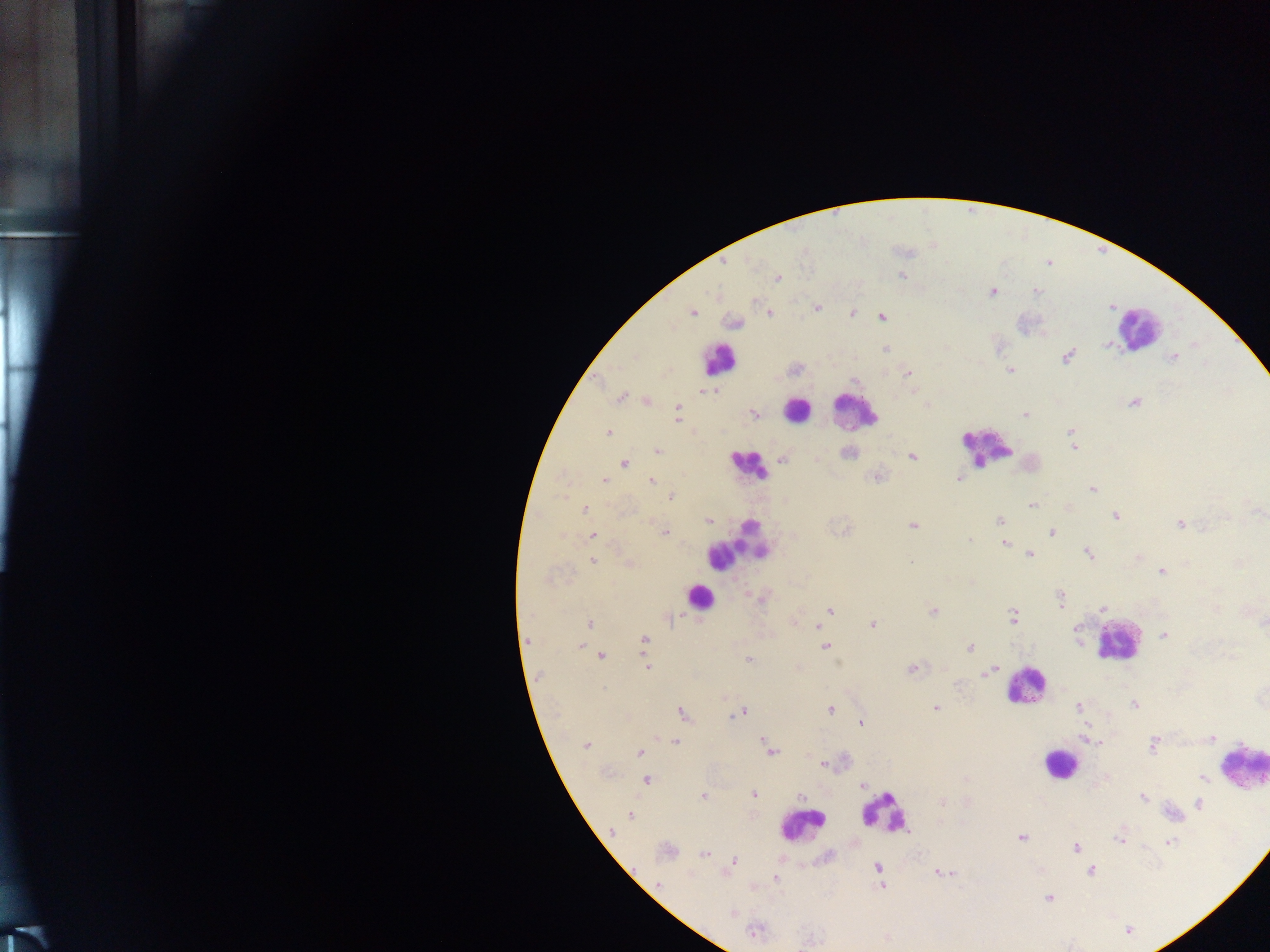

Approximate centers as x y in pixels.
Summary:
  - Malaria parasite locations: 902 276; 777 278; 992 292; 1037 292; 817 307; 693 312; 769 313; 852 313; 882 317; 733 322; 1106 345; 885 349; 1067 356; 1173 357; 795 369; 1009 371; 907 374; 701 391; 713 391; 620 397; 648 402; 1134 403; 677 407; 754 414; 1025 414; 677 419; 1071 431; 608 432; 1073 446; 658 451; 848 452; 912 457; 782 459; 816 460; 624 463; 877 477; 959 478; 604 481; 651 481; 1092 489; 671 497; 1031 505; 584 509; 1257 512; 1115 516; 999 520; 709 522; 1180 524; 912 526; 665 533; 1051 533; 594 536; 970 540; 1004 543; 1029 554; 1088 554; 1138 557; 593 560; 910 562; 629 563; 1186 564; 1162 572; 1061 599; 1103 608; 1216 608; 830 611; 933 611; 1012 617; 671 618; 589 623; 873 624; 1264 624; 818 626; 1164 635; 645 640; 581 646; 825 647; 969 648; 602 655; 748 659; 647 667; 911 669; 990 671; 724 698; 1134 705; 1079 707; 830 708; 936 708; 742 712; 683 714; 860 723; 1211 738; 1088 740; 764 741; 675 742; 1153 745; 586 746; 770 751; 639 754; 824 764; 647 780; 1208 782; 862 785; 754 794; 703 796; 801 796; 1142 797; 941 802; 1199 803; 630 816; 612 831; 1021 838; 1119 839; 1170 842; 1076 847; 666 852; 704 854; 733 861; 877 866; 1091 871; 945 872; 775 878; 658 884; 882 885; 1049 898; 732 914; 754 932
  - Leukocyte locations: 1139 328; 719 359; 797 409; 854 410; 989 446; 747 465; 736 546; 698 596; 1116 640; 1025 686; 1244 758; 1058 764; 884 812; 800 824
  - Capture: mobile-phone photograph through a microscope
  - Preparation: thick blood smear
  - Image size: 1270×952 pixels
  - Field of view: single
  - Country: Ghana